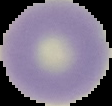
preparation = thin blood smear
image size = 112×106 pixels
result = no Plasmodium parasites seen
image type = cell region segmented out of the field of view; surrounding area masked to black